Identify the blood parasite species.
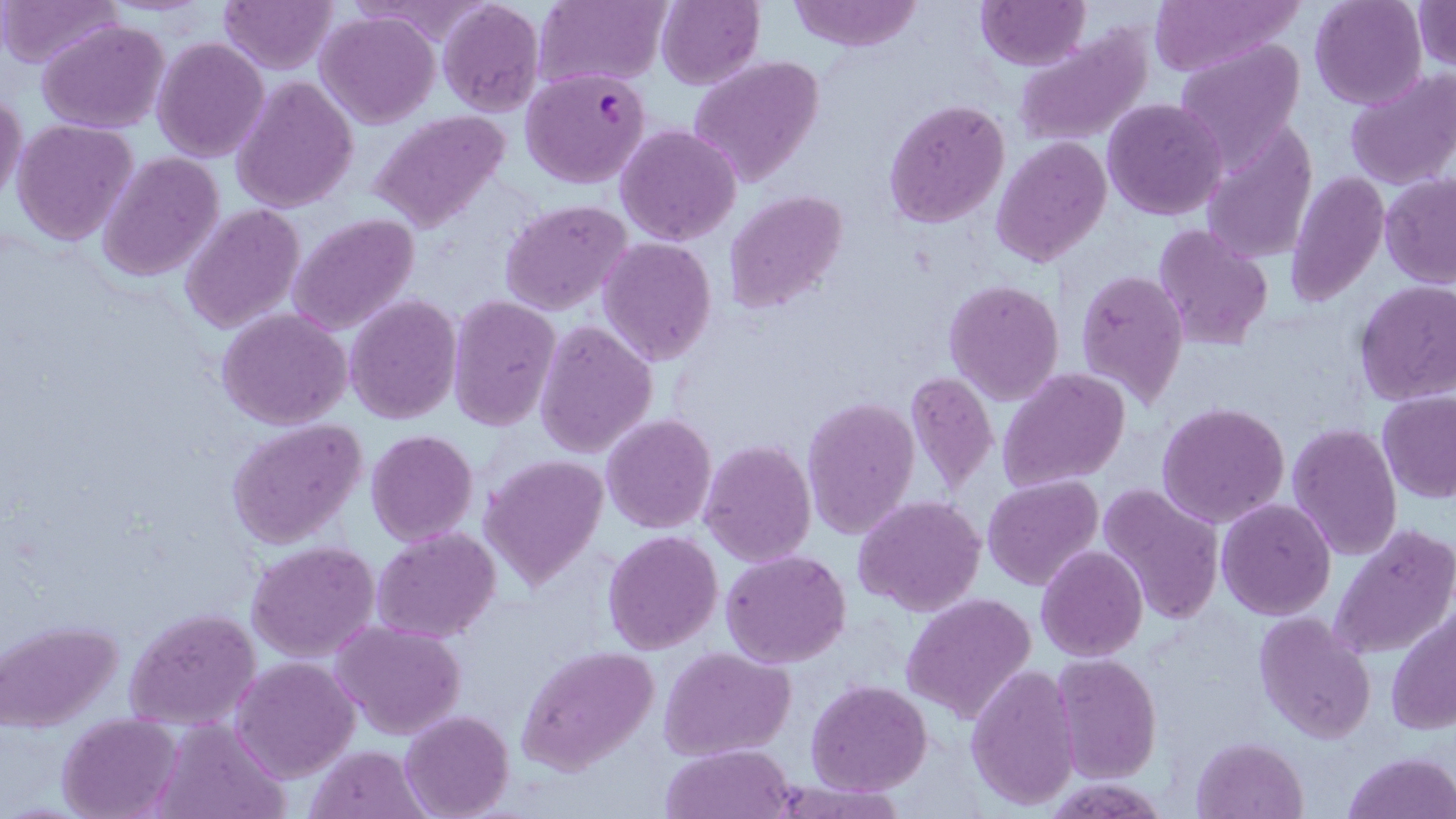

Plasmodium falciparum.

Approximate bounding boxes as [x1, y1, x2, y2] in pixels. Plasmodium falciparum-infected red blood cell locations: [520, 67, 651, 188]. Uninfected red blood cell locations: [0, 0, 122, 69], [533, 0, 670, 89], [787, 0, 923, 52], [1142, 0, 1305, 78], [1309, 0, 1428, 110], [1412, 0, 1455, 72], [219, 1, 337, 73], [437, 1, 544, 118], [655, 1, 765, 89], [976, 1, 1087, 70], [317, 10, 438, 128], [38, 19, 170, 133], [1013, 26, 1154, 146], [152, 36, 271, 161], [1175, 38, 1307, 168], [687, 56, 826, 188], [1343, 68, 1456, 191], [232, 75, 359, 213], [0, 91, 26, 207], [1103, 97, 1229, 220], [883, 98, 1010, 229], [366, 109, 513, 232], [11, 119, 138, 248], [616, 124, 742, 246], [1199, 124, 1319, 264], [992, 136, 1111, 266], [97, 152, 224, 283], [1285, 173, 1389, 304], [1380, 173, 1456, 288], [725, 190, 848, 314], [501, 200, 634, 315], [180, 205, 305, 334], [287, 214, 419, 335], [1153, 223, 1275, 350], [598, 237, 718, 365], [1075, 268, 1189, 412], [944, 279, 1066, 406], [1354, 281, 1456, 405], [346, 295, 461, 425], [446, 295, 560, 431], [217, 308, 352, 430], [533, 320, 658, 458], [999, 369, 1131, 494], [903, 370, 998, 496], [1377, 392, 1456, 504], [802, 396, 920, 540], [1156, 401, 1290, 528], [602, 413, 716, 533], [227, 418, 370, 551], [1286, 420, 1401, 562], [366, 429, 480, 545], [699, 439, 816, 567], [480, 456, 607, 588], [983, 475, 1104, 592], [1096, 482, 1225, 627], [853, 495, 987, 618], [1216, 498, 1336, 620], [1329, 523, 1455, 662], [372, 526, 501, 644], [602, 531, 723, 656], [246, 540, 380, 662], [1036, 545, 1148, 663], [720, 548, 852, 668], [903, 593, 1037, 724], [124, 605, 262, 731], [1387, 607, 1456, 738], [1254, 611, 1377, 743], [3, 619, 122, 732], [332, 620, 466, 740], [516, 644, 661, 774], [658, 645, 797, 762], [1050, 653, 1163, 786], [230, 656, 360, 782], [966, 662, 1081, 810], [806, 679, 932, 795], [400, 711, 514, 819], [58, 714, 181, 819], [150, 719, 290, 819], [1192, 736, 1307, 818], [663, 743, 795, 819], [305, 745, 434, 819], [1341, 750, 1456, 819]. One field of a larger specimen. Thin blood film. 1000x magnification. May-Grünwald-Giemsa stain. Image is 1456×819 pixels. Light microscopy.